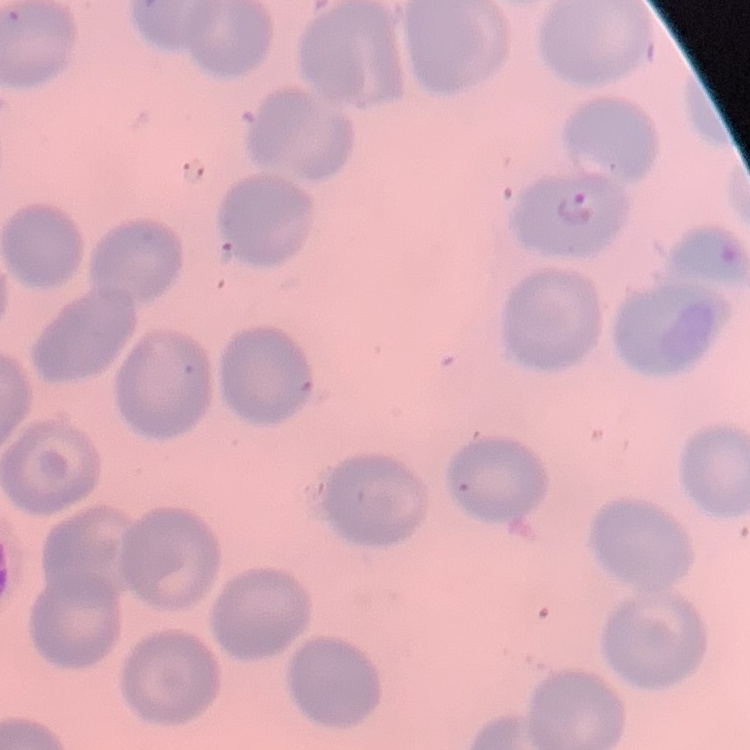

erythrocyte morphology = no rouleaux formation
stain = Field's or Giemsa
image type = square crop of a larger photomicrograph
preparation = thin blood film